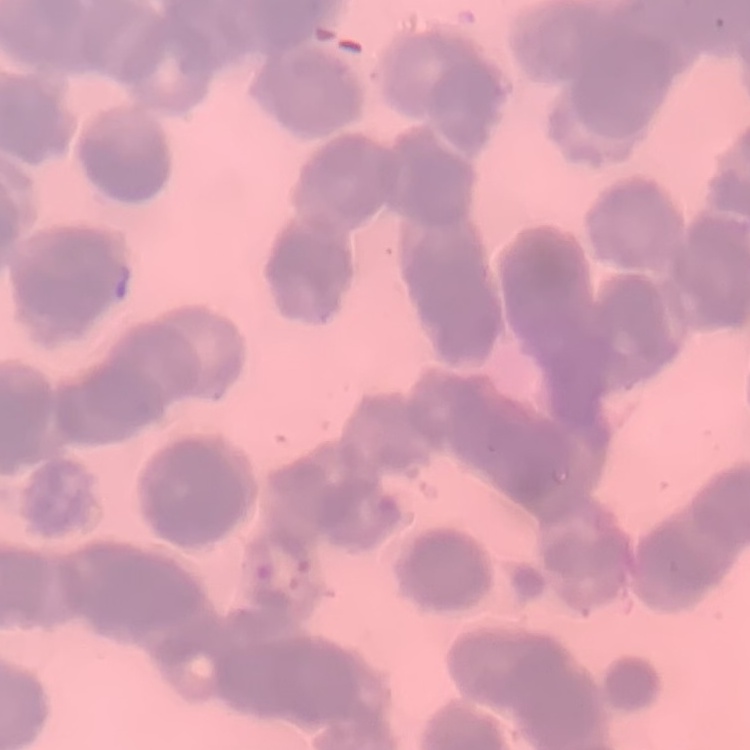 The red blood cells exhibit rouleaux formation. Stained with either Field's or Giemsa. One tile cut from a larger photomicrograph. Thin peripheral smear.